Report the malaria status of this cell.
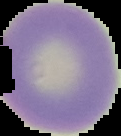
Uninfected.

Summary:
  - Image type: cell region segmented out of the field of view; surrounding area masked to black
  - Preparation: thin blood film
  - Image size: 121×136 pixels